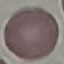

result = no malaria parasites detected
capture = smartphone through the microscope eyepiece
image type = cell patch, automatically extracted from a larger field of view and resized to 64 × 64 pixels
stain = Giemsa
preparation = thin blood smear